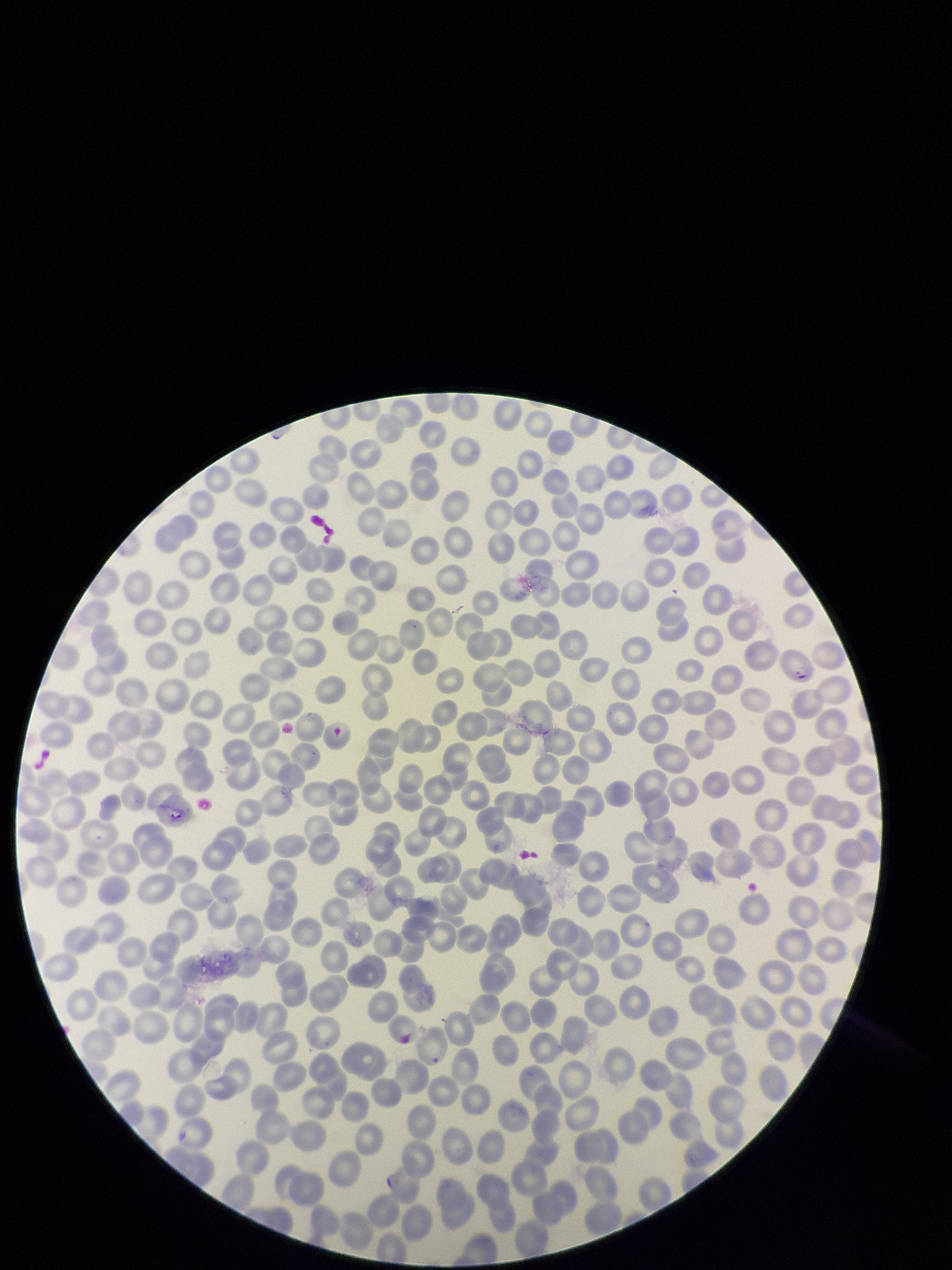

Parasitized red blood cell count: 2. Patient malaria status: positive. Giemsa stain. One field from this slide. Red blood cell count: 309. Species reported for this patient: Plasmodium falciparum. Photographed through the microscope eyepiece with a smartphone camera. Parasitized red blood cells: detected. Preparation: thin. Image is 952×1270 pixels.